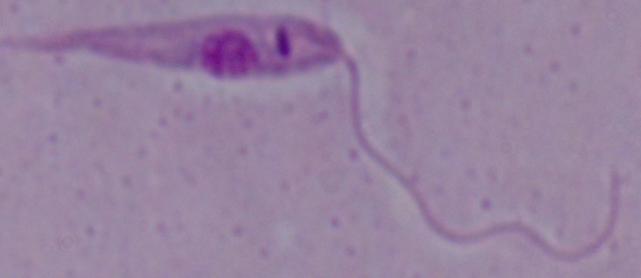

modality = micrograph
magnification = 1000x
identification = Leishmania